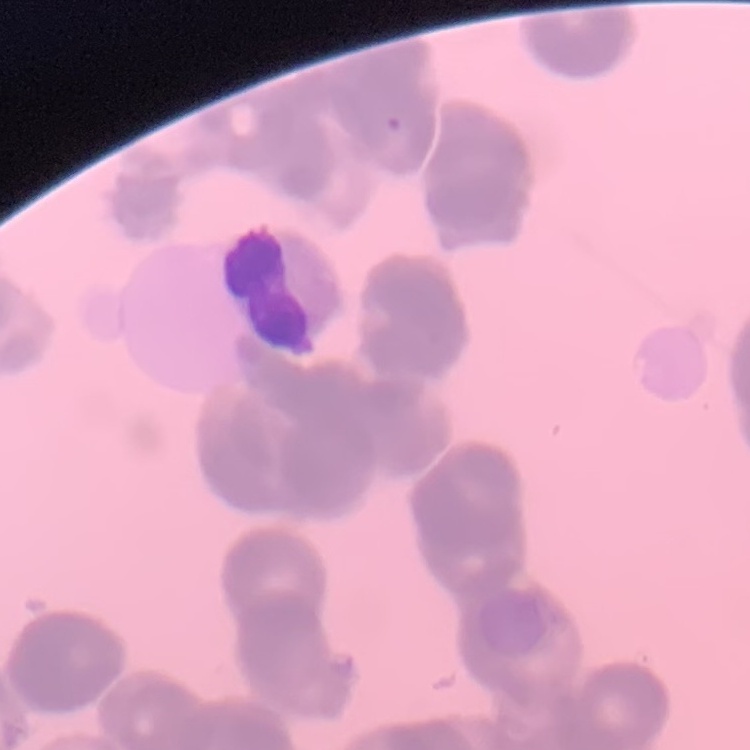

The erythrocytes show rouleaux formation. One tile cut from a larger photomicrograph. Thin blood film. Field's or Giemsa stain.